Describe the morphology of the red blood cells.
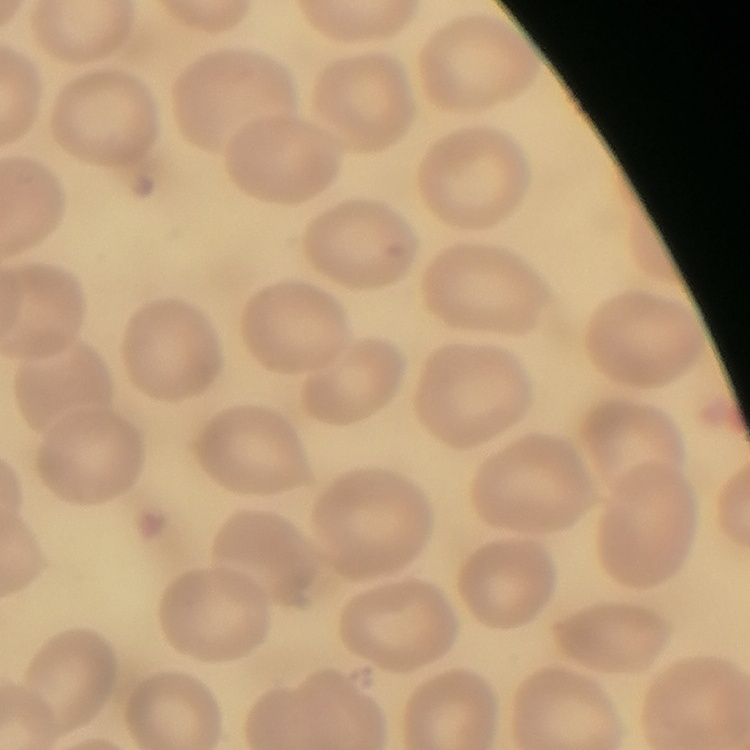

They show no rouleaux formation.

stain = Field's or Giemsa
image type = one tile cut from a larger photomicrograph
preparation = thin peripheral smear